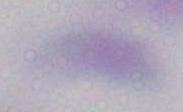
modality = photomicrograph
identification = Toxoplasma gondii
magnification = 1000x